Report the malaria status of this cell.
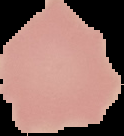

Uninfected.

From a thin blood smear. Image is 124×136 pixels. Segmented cell region on a black background.